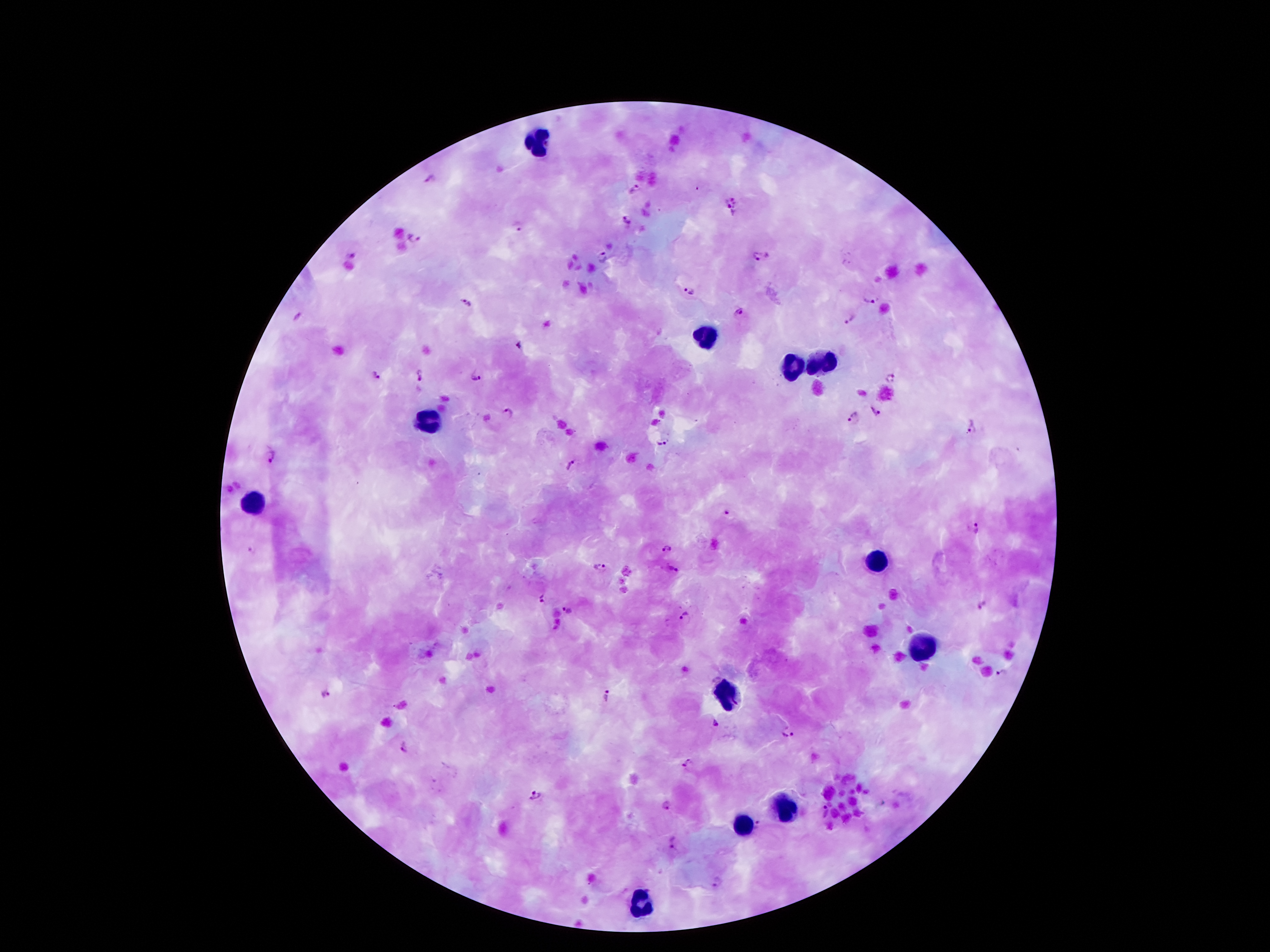

Approximate centers as [x, y] in pixels.
Summary:
  - Leukocyte locations: [537, 139], [705, 337], [823, 364], [789, 366], [430, 421], [251, 500], [875, 559], [920, 647], [724, 687], [783, 811], [743, 822], [640, 904]
  - Plasmodium parasite locations: [432, 179], [634, 191], [736, 201], [726, 204], [628, 219], [517, 227], [413, 239], [351, 253], [756, 257], [602, 258], [689, 292], [871, 296], [466, 303], [739, 313], [297, 319], [852, 319], [520, 347], [420, 375], [377, 377], [477, 377], [890, 377], [875, 410], [509, 413], [853, 416], [971, 428], [664, 442], [269, 455], [574, 464], [727, 513], [978, 529], [667, 549], [251, 550], [599, 567], [673, 567], [542, 598], [979, 605], [568, 609], [684, 617], [1003, 675], [326, 693], [609, 698], [716, 724], [788, 734], [405, 743], [689, 765], [536, 795], [667, 805], [823, 812], [671, 843], [717, 883]
  - Capture: smartphone camera through the microscope eyepiece
  - Stain: Giemsa
  - Image size: 1270×952 pixels
  - Patient malaria status: infected with Plasmodium falciparum
  - Magnification: 100x
  - Preparation: thick peripheral-blood smear
  - Field of view: one from this slide